Classify this cell by malaria status.
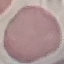

Uninfected.

stain: Giemsa
image_type: automatically extracted cell patch, resized to 64 × 64 pixels
preparation: thin blood smear
capture: smartphone camera at the microscope eyepiece